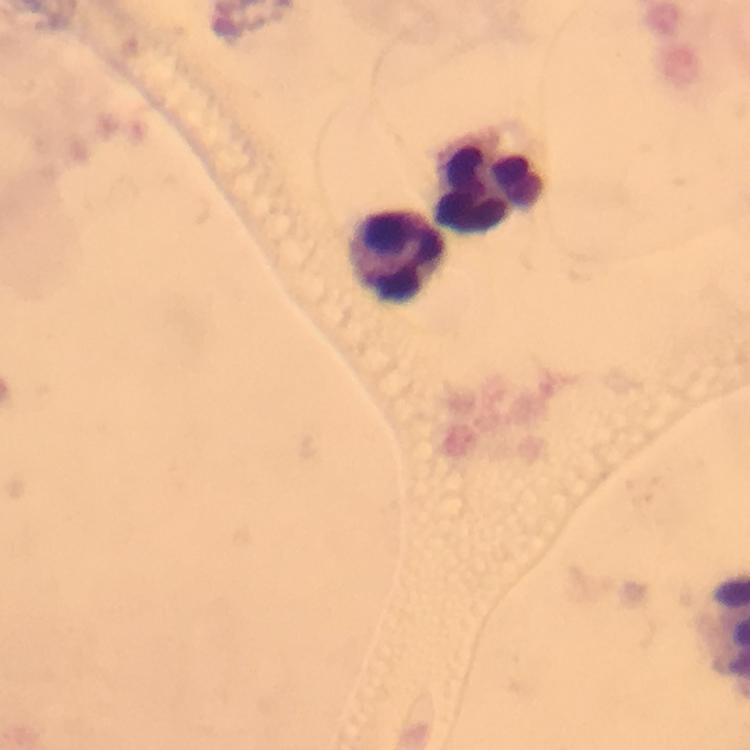

Approximate centers as [x, y] in pixels.
Summary:
  - Leukocyte locations: [487, 179], [395, 253]
  - Context: from a diagnostic examination for malaria
  - Image size: 750×750 pixels
  - Stain: Giemsa
  - Plasmodium parasites: none detected
  - Preparation: thick blood film
  - Immersion oil: used
  - Cropped from: a single field of view
  - Capture: smartphone photograph through a microscope
  - Magnification: 100x